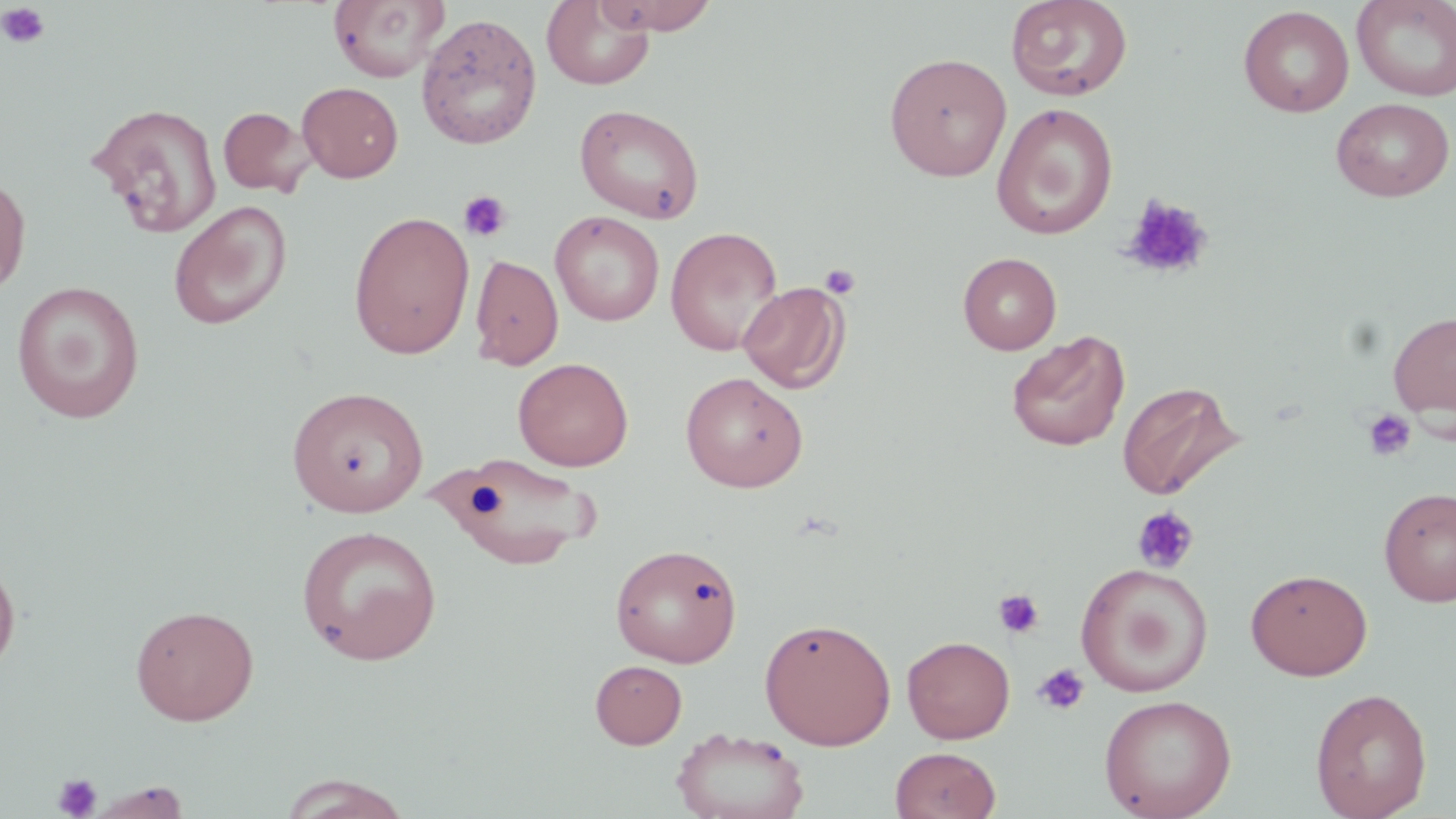

Summary:
  - Coordinate format: approximate bounding boxes as [x1, y1, x2, y2] in pixels
  - Uninfected red blood cell locations: [327, 0, 449, 82], [542, 0, 655, 90], [594, 0, 720, 35], [1005, 0, 1133, 101], [1352, 0, 1456, 101], [1238, 5, 1355, 117], [416, 13, 542, 151], [884, 52, 1012, 181], [297, 81, 403, 183], [1331, 97, 1454, 202], [87, 102, 223, 239], [991, 102, 1118, 239], [574, 103, 704, 224], [218, 106, 312, 197], [0, 170, 31, 299], [168, 200, 292, 330], [348, 210, 475, 359], [550, 210, 664, 326], [665, 225, 783, 357], [958, 252, 1061, 354], [470, 254, 563, 370], [11, 281, 145, 422], [738, 281, 850, 394], [1388, 309, 1456, 425], [1007, 330, 1130, 452], [513, 357, 633, 471], [680, 371, 808, 492], [1117, 380, 1242, 501], [287, 386, 429, 517], [439, 453, 602, 569], [1379, 486, 1456, 607], [295, 524, 443, 665], [609, 542, 744, 667], [0, 556, 21, 680], [1075, 561, 1213, 697], [1245, 568, 1373, 680], [130, 604, 259, 725], [759, 617, 896, 749], [902, 635, 1015, 743], [590, 660, 687, 748], [1310, 687, 1432, 819], [1098, 694, 1237, 819], [670, 727, 811, 819], [890, 746, 1001, 819], [275, 774, 415, 819], [88, 781, 191, 818]
  - Platelet locations: [1, 3, 51, 49], [457, 190, 513, 243], [1122, 194, 1214, 281], [819, 263, 861, 300], [1362, 408, 1418, 462], [1132, 505, 1200, 575], [993, 589, 1045, 639], [1033, 662, 1090, 716], [53, 772, 101, 818]
  - Slide-level diagnosis: negative for blood parasites
  - Modality: optical microscopy
  - Field of view: single
  - Image size: 1456×819 pixels
  - Preparation: thin blood film
  - Stain: May-Grünwald-Giemsa
  - Magnification: 1000x